Locate every leukocyte (white blood cell).
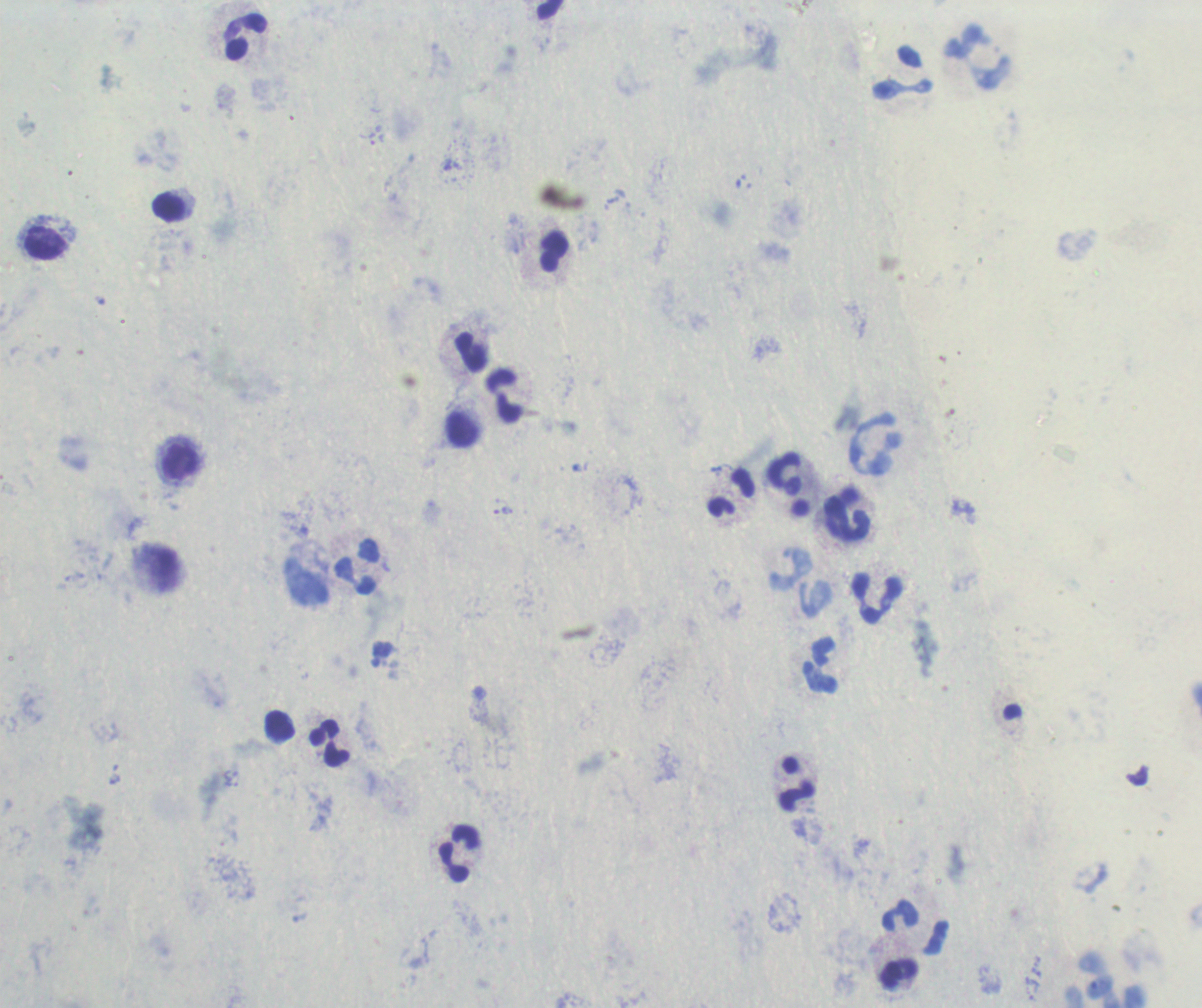
Approximate object centers, in pixels from the top-left corner.
Leukocytes: (x=246, y=38), (x=978, y=59), (x=903, y=72), (x=169, y=207), (x=47, y=243), (x=554, y=252), (x=471, y=353), (x=504, y=396), (x=462, y=430), (x=876, y=446), (x=180, y=461), (x=784, y=475), (x=732, y=494), (x=846, y=515), (x=357, y=566), (x=306, y=583), (x=877, y=599), (x=820, y=666), (x=279, y=725), (x=329, y=743), (x=797, y=784), (x=460, y=854), (x=916, y=928), (x=897, y=974), (x=1108, y=982).

magnification = 100x
stain = Romanowsky
image size = 1202×1008 pixels
field of view = single
result = no malaria parasites detected
preparation = thick blood smear
background quality = poor
context = previously used in an actual diagnosis